Name the cell type shown.
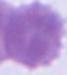
An erythrocyte.

magnification = 1000x
modality = micrograph